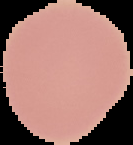

Summary:
  - Result: no Plasmodium parasites detected
  - Preparation: thin blood film
  - Image size: 133×145 pixels
  - Image type: segmented cell region with the area outside set to black